Outline platelets.
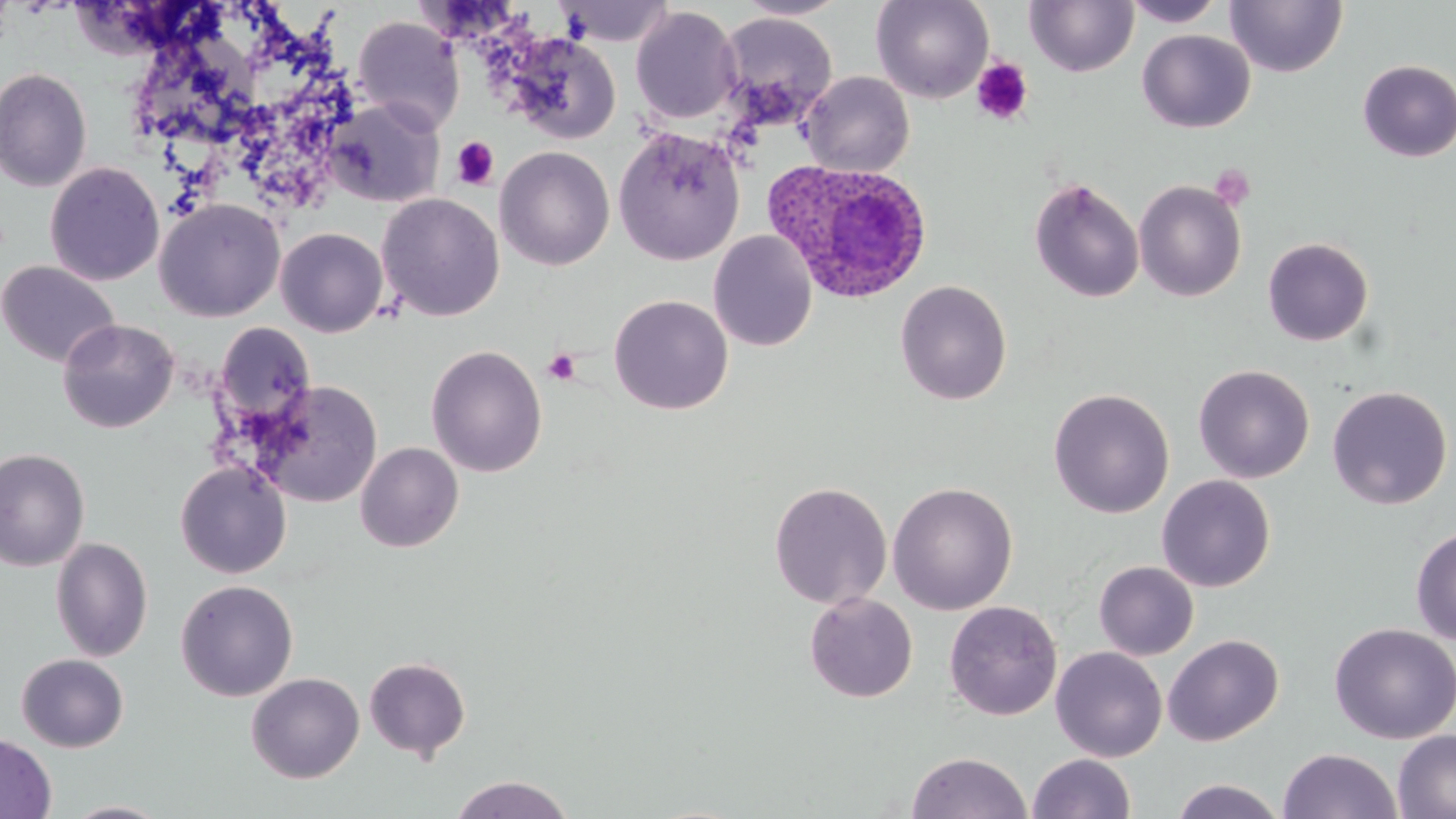
Approximate bounding boxes as (x1, y1, x2, y2) in pixels.
Platelets: (970, 58, 1033, 125), (451, 137, 499, 190), (1210, 164, 1256, 211), (543, 349, 581, 386).

Uninfected red blood cell locations: (733, 0, 849, 21), (871, 0, 995, 103), (1122, 0, 1227, 27), (554, 1, 674, 46), (1024, 1, 1139, 78), (1225, 1, 1347, 77), (630, 6, 743, 125), (717, 12, 838, 127), (353, 16, 465, 134), (1137, 29, 1255, 132), (506, 32, 621, 144), (1357, 59, 1456, 163), (0, 67, 93, 192), (801, 71, 915, 177), (324, 99, 445, 207), (613, 127, 745, 265), (494, 146, 615, 270), (45, 161, 165, 286), (1028, 177, 1144, 303), (1134, 180, 1247, 302), (376, 193, 504, 321), (153, 198, 285, 321), (276, 227, 388, 337), (708, 230, 818, 351), (1262, 237, 1374, 347), (0, 260, 121, 368), (895, 279, 1012, 405), (608, 294, 733, 415), (57, 318, 179, 433), (212, 322, 317, 430), (426, 345, 547, 477), (1193, 364, 1315, 482), (251, 381, 383, 507), (1326, 385, 1453, 510), (1048, 388, 1175, 518), (355, 442, 464, 552), (0, 447, 91, 571), (175, 461, 292, 579), (1156, 475, 1276, 592), (768, 481, 893, 609), (887, 481, 1019, 615), (1410, 525, 1456, 644), (50, 536, 154, 662), (1094, 560, 1199, 660), (175, 579, 299, 701), (804, 592, 918, 702), (944, 599, 1063, 720), (1329, 622, 1456, 744), (1162, 634, 1284, 746), (1050, 647, 1167, 761), (16, 653, 129, 752), (364, 656, 471, 761), (246, 672, 364, 783), (1393, 729, 1456, 818), (0, 732, 57, 819), (1278, 748, 1403, 819), (907, 751, 1032, 819), (1027, 753, 1136, 819), (449, 774, 575, 819), (1169, 779, 1287, 818), (62, 801, 173, 819). Plasmodium ovale-infected red blood cell locations: (763, 161, 934, 304). Slide-level diagnosis: Plasmodium ovale. 1000x magnification. Thin blood film. Light microscopy. Image is 1456×819 pixels. One field of a larger specimen. May-Grünwald-Giemsa-stained preparation.